Report the malaria status of this cell.
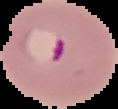
It is parasitized.

Cell region segmented out of the field of view; the surrounding area is masked to black. From a thin blood film. Image is 118×109 pixels.